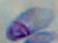

Micrograph. Toxoplasma gondii is seen. Captured at 1000x magnification.